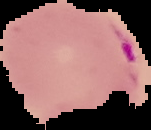
malaria status = parasitized
image size = 151×130 pixels
preparation = thin blood film
image type = cell region segmented out of the field of view; surrounding area masked to black